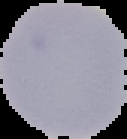
From a thin blood smear. Result: no malaria parasites seen. Image is 127×139 pixels. The area outside the segmented cell region is set to black.